Report the malaria status of this cell.
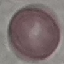

Uninfected.

image_type: cell patch, automatically extracted from a larger field of view and resized to 64 × 64 pixels
capture: smartphone camera at the microscope eyepiece
stain: Giemsa
preparation: thin smear